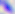

identification = Toxoplasma gondii
magnification = 400x
modality = photomicrograph